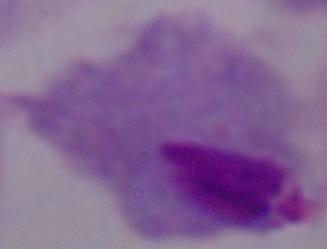

Summary:
  - Identification: trichomonad
  - Modality: photomicrograph
  - Magnification: 1000x